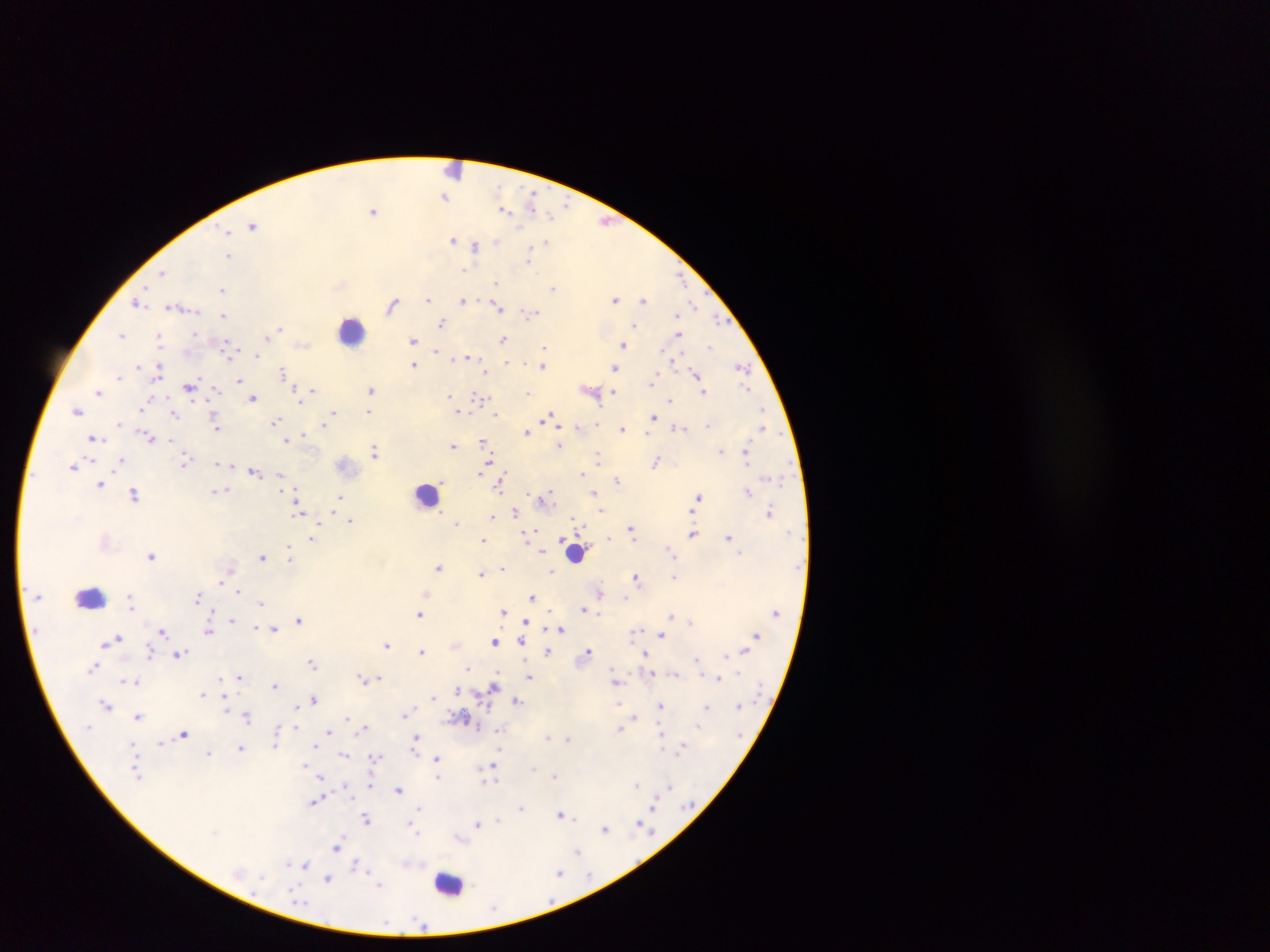 Approximate centers as (x, y) in pixels. Object labeled both Plasmodium parasite and leukocyte by the source: (455, 170). Leukocyte locations: (352, 328), (427, 494), (576, 552), (90, 597), (450, 884). Plasmodium parasite locations: (445, 196), (532, 200), (505, 209), (374, 210), (552, 215), (607, 221), (253, 224), (227, 233), (454, 239), (496, 241), (546, 243), (476, 246), (529, 254), (229, 255), (464, 270), (162, 271), (681, 278), (496, 282), (553, 288), (223, 289), (428, 298), (463, 299), (615, 299), (643, 300), (138, 302), (392, 304), (498, 305), (175, 306), (694, 306), (531, 313), (679, 313), (223, 315), (442, 322), (635, 324), (280, 327), (195, 333), (680, 333), (121, 334), (266, 336), (504, 338), (160, 339), (413, 340), (303, 344), (624, 344), (712, 345), (544, 346), (436, 351), (256, 354), (468, 357), (507, 362), (415, 364), (543, 365), (138, 366), (160, 366), (615, 367), (742, 367), (283, 372), (487, 372), (697, 375), (119, 376), (240, 380), (653, 381), (190, 386), (216, 389), (371, 389), (296, 390), (590, 390), (313, 391), (703, 391), (99, 392), (529, 392), (614, 393), (450, 394), (253, 397), (480, 397), (151, 399), (669, 400), (144, 404), (763, 409), (77, 410), (370, 411), (458, 411), (175, 412), (334, 412), (497, 414), (654, 415), (549, 417), (276, 420), (119, 423), (323, 424), (709, 424), (217, 426), (579, 427), (678, 427), (763, 428), (622, 429), (527, 431), (647, 433), (304, 434), (94, 438), (151, 438), (288, 439), (482, 440), (172, 441), (454, 445), (560, 446), (375, 451), (721, 451), (747, 452), (598, 456), (121, 460), (186, 461), (656, 462), (216, 463), (73, 465), (233, 465), (487, 465), (253, 471), (583, 472), (280, 474), (618, 480), (101, 483), (500, 484), (295, 486), (222, 490), (594, 492), (748, 492), (134, 493), (339, 495), (699, 497), (543, 498), (299, 507), (600, 511), (515, 512), (770, 512), (334, 515), (517, 516), (492, 517), (576, 519), (351, 520), (457, 522), (631, 528), (537, 530), (693, 534), (528, 535), (728, 537), (314, 538), (483, 540), (544, 550), (670, 550), (151, 556), (263, 556), (291, 556), (439, 566), (504, 566), (229, 569), (552, 569), (481, 572), (674, 576), (636, 577), (220, 580), (238, 591), (600, 591), (425, 592), (198, 596), (532, 597), (261, 603), (131, 604), (583, 609), (503, 612), (672, 613), (420, 615), (298, 619), (233, 620), (526, 621), (691, 622), (273, 628), (561, 629), (163, 630), (208, 630), (635, 631), (661, 634), (756, 635), (118, 638), (495, 640), (110, 641), (521, 641), (386, 644), (456, 645), (104, 646), (149, 650), (744, 650), (423, 651), (548, 651), (588, 651), (178, 652), (645, 653), (726, 655), (696, 660), (313, 664), (93, 667), (467, 668), (675, 674), (529, 676), (240, 677), (717, 677), (219, 678), (364, 678), (377, 679), (122, 680), (616, 681), (138, 682), (274, 684), (494, 685), (457, 690), (202, 693), (433, 696), (224, 697), (314, 699), (516, 699), (620, 703), (107, 705), (661, 705), (707, 707), (297, 708), (226, 710), (405, 714), (247, 715), (139, 716), (635, 717), (346, 718), (464, 718), (297, 725), (365, 727), (622, 727), (278, 729), (498, 729), (329, 732), (185, 733), (416, 736), (548, 736), (663, 736), (569, 739), (132, 742), (161, 742), (275, 744), (315, 746), (683, 746), (241, 748), (663, 749), (209, 751), (344, 755), (416, 755), (436, 757), (372, 758), (495, 764), (306, 765), (553, 774), (438, 775), (322, 776), (492, 781), (370, 784), (637, 785), (346, 786), (669, 787), (398, 788), (315, 800), (655, 804), (520, 808), (561, 813), (367, 818), (498, 821), (411, 822), (640, 822), (478, 824), (605, 829), (415, 831), (459, 837), (338, 845), (578, 852), (289, 862), (356, 864), (305, 865), (560, 873), (329, 878), (379, 885). Image is 1270×952 pixels. Sample from Ghana. Thick blood film. Single field of view. Photographed through a microscope with a mobile-phone camera.